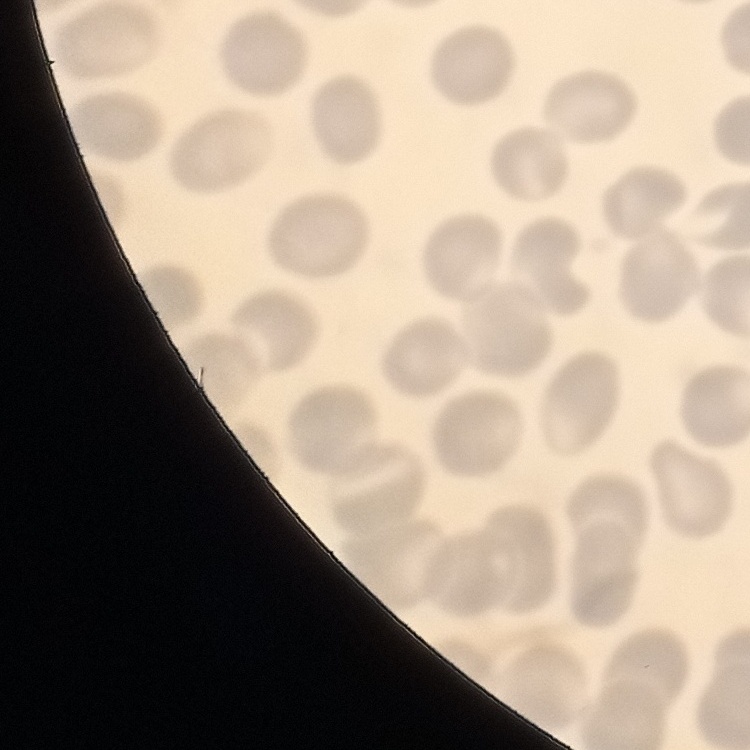

red_blood_cell_morphology: no rouleaux formation
image_type: square crop of a larger photomicrograph
preparation: thin blood film
stain: Field's or Giemsa